Identify the parasite.
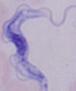

This is a trypanosome.

Summary:
  - Magnification: 1000x
  - Modality: photomicrograph